Outline each Plasmodium falciparum-infected red blood cell.
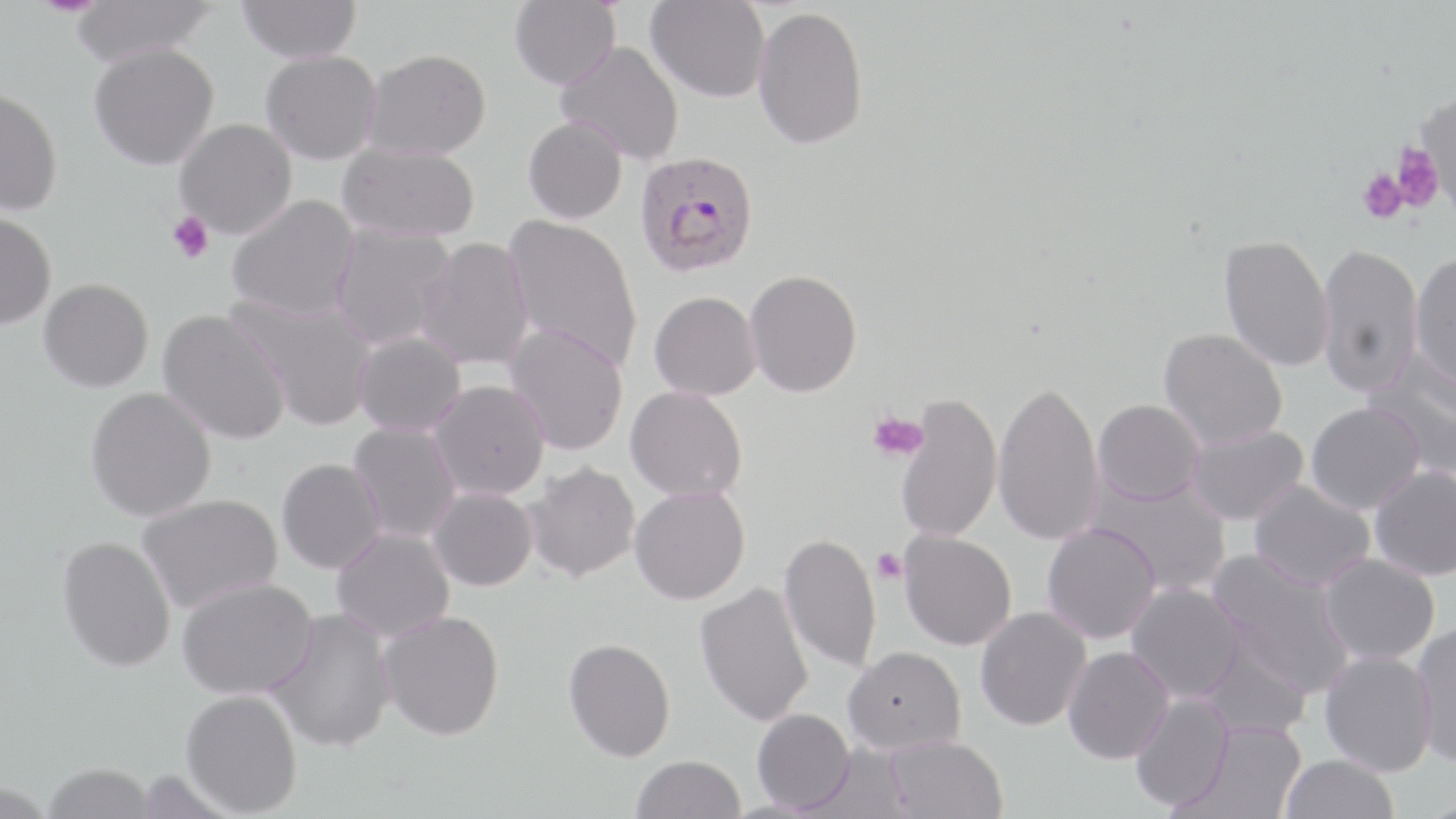
Approximate bounding boxes as (x1, y1, x2, y2) in pixels.
Plasmodium falciparum-infected red blood cells: (634, 153, 761, 281).

slide-level diagnosis = Plasmodium falciparum
modality = light microscopy
platelet locations = approximate bounding boxes as (x1, y1, x2, y2) in pixels: (1390, 142, 1444, 212), (1357, 167, 1408, 225), (167, 210, 214, 264), (866, 410, 929, 462), (872, 548, 908, 585)
field of view = single
uninfected red blood cell locations = approximate bounding boxes as (x1, y1, x2, y2) in pixels: (69, 0, 222, 70), (236, 0, 362, 66), (510, 0, 621, 92), (646, 0, 770, 104), (752, 7, 868, 153), (554, 41, 684, 166), (90, 46, 219, 174), (261, 52, 381, 167), (362, 52, 491, 163), (0, 92, 61, 219), (1413, 92, 1456, 213), (523, 117, 628, 226), (174, 120, 297, 241), (337, 144, 479, 244), (228, 195, 360, 323), (0, 213, 55, 333), (501, 214, 641, 371), (331, 222, 455, 350), (1218, 235, 1334, 373), (416, 237, 535, 372), (1316, 244, 1423, 399), (1409, 254, 1456, 393), (744, 271, 863, 399), (38, 281, 153, 396), (229, 291, 378, 432), (649, 293, 761, 402), (156, 310, 291, 447), (503, 324, 629, 457), (1158, 329, 1287, 451), (353, 332, 466, 438), (1365, 355, 1456, 483), (426, 382, 550, 502), (992, 382, 1105, 546), (625, 387, 747, 504), (85, 389, 216, 524), (895, 395, 1003, 543), (1093, 401, 1205, 507), (1306, 404, 1424, 515), (348, 422, 462, 542), (1186, 425, 1308, 526), (277, 459, 386, 576), (522, 463, 641, 586), (1369, 466, 1456, 582), (1086, 474, 1232, 595), (1249, 479, 1375, 592), (629, 487, 751, 607), (427, 488, 538, 594), (137, 495, 283, 615), (1042, 524, 1160, 644), (332, 527, 455, 643), (898, 530, 1016, 651), (778, 534, 882, 674), (56, 537, 176, 675), (1206, 549, 1357, 697), (1318, 554, 1440, 665), (177, 579, 318, 701), (1126, 582, 1245, 703), (694, 583, 814, 728), (975, 606, 1092, 732), (264, 609, 396, 756), (378, 612, 505, 745), (1410, 621, 1456, 768), (1198, 637, 1312, 739), (563, 640, 675, 765), (844, 646, 966, 756), (1063, 646, 1175, 765), (1319, 650, 1437, 777), (180, 692, 302, 818), (1130, 692, 1234, 813), (752, 709, 855, 814), (1185, 721, 1306, 819), (884, 737, 1008, 819), (1280, 755, 1399, 819), (631, 757, 746, 819), (41, 766, 157, 819), (0, 785, 56, 819)
magnification = 1000x
preparation = thin blood smear
stain = May-Grünwald-Giemsa
image size = 1456×819 pixels